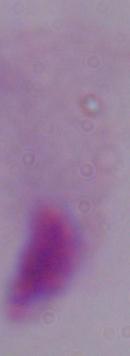

{
  "magnification": "1000x",
  "modality": "micrograph",
  "identification": "trichomonad"
}